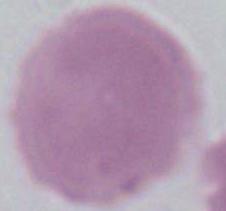

modality = micrograph
identification = erythrocyte
magnification = 1000x